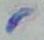
identification = Toxoplasma gondii
magnification = 1000x
modality = micrograph